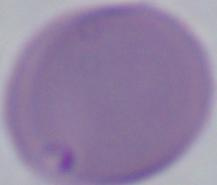

{
  "identification": "Babesia",
  "modality": "micrograph",
  "magnification": "1000x"
}